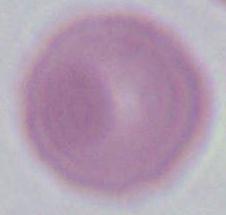 Photomicrograph. Captured at 1000x magnification. A red blood cell is seen.